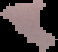

Image is 58×52 pixels. The area outside the segmented cell region is set to black. Result: Plasmodium parasites detected. From a thin blood film.